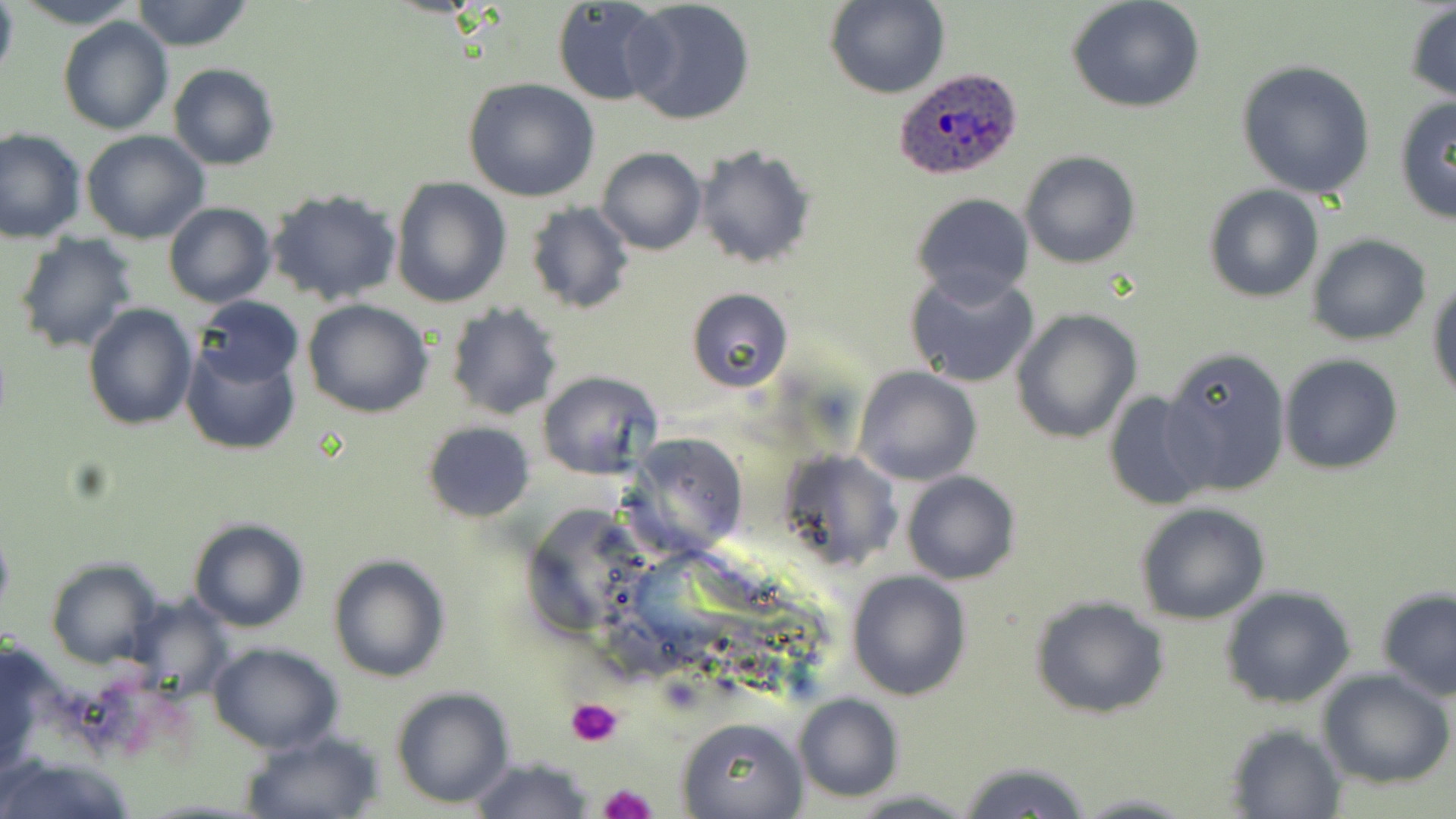
slide_level_diagnosis: Plasmodium ovale
modality: light microscopy
magnification: 1000x
uninfected_red_blood_cell_locations: 'approximate bounding boxes as [x1, y1, x2, y2] in pixels: [0, 0, 18, 86], [12, 0, 142, 29], [129, 0, 255, 52], [825, 0, 949, 100], [549, 1, 672, 107], [621, 1, 758, 126], [1066, 1, 1207, 113], [1403, 4, 1456, 105], [58, 16, 174, 135], [1237, 60, 1375, 199], [168, 63, 280, 171], [462, 78, 600, 203], [1392, 97, 1456, 225], [0, 127, 86, 243], [80, 130, 209, 243], [693, 146, 816, 268], [596, 147, 706, 256], [1020, 150, 1141, 270], [389, 177, 511, 307], [1204, 184, 1325, 302], [266, 188, 404, 307], [909, 192, 1036, 305], [163, 202, 276, 308], [524, 202, 635, 316], [11, 233, 140, 354], [1308, 234, 1431, 346], [904, 270, 1039, 388], [1428, 278, 1456, 405], [686, 287, 794, 394], [195, 296, 303, 389], [301, 300, 434, 420], [444, 302, 563, 422], [81, 303, 197, 432], [1011, 308, 1143, 444], [181, 339, 301, 456], [1160, 346, 1292, 498], [1279, 354, 1404, 476], [853, 365, 982, 485], [537, 370, 663, 480], [1102, 391, 1216, 514], [423, 420, 537, 521], [622, 432, 749, 555], [778, 447, 901, 570], [901, 471, 1020, 585], [1134, 502, 1273, 625], [187, 517, 310, 633], [326, 553, 451, 683], [45, 559, 164, 669], [846, 570, 969, 701], [1376, 585, 1456, 701], [1221, 587, 1356, 710], [1028, 596, 1171, 720], [125, 600, 233, 700], [1, 640, 52, 778], [207, 641, 343, 755], [1317, 669, 1456, 789], [390, 686, 515, 808], [792, 692, 903, 803], [679, 716, 808, 818], [1225, 724, 1347, 817], [241, 730, 385, 818], [0, 756, 141, 819], [469, 757, 594, 819], [957, 760, 1093, 819], [845, 789, 979, 819], [1065, 792, 1202, 818]'
preparation: thin blood film
image_size: 1456×819 pixels
plasmodium_ovale_infected_red_blood_cell_locations: 'approximate bounding boxes as [x1, y1, x2, y2] in pixels: [892, 68, 1023, 179]'
stain: May-Grünwald-Giemsa
platelet_locations: 'approximate bounding boxes as [x1, y1, x2, y2] in pixels: [566, 699, 625, 747], [599, 783, 658, 819]'
field_of_view: single